Assess this cell for malaria.
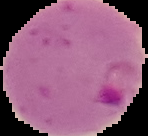
It is parasitized.

Image is 148×136 pixels. Segmented cell region on a black background. From a thin blood smear.